Mark where platelets are.
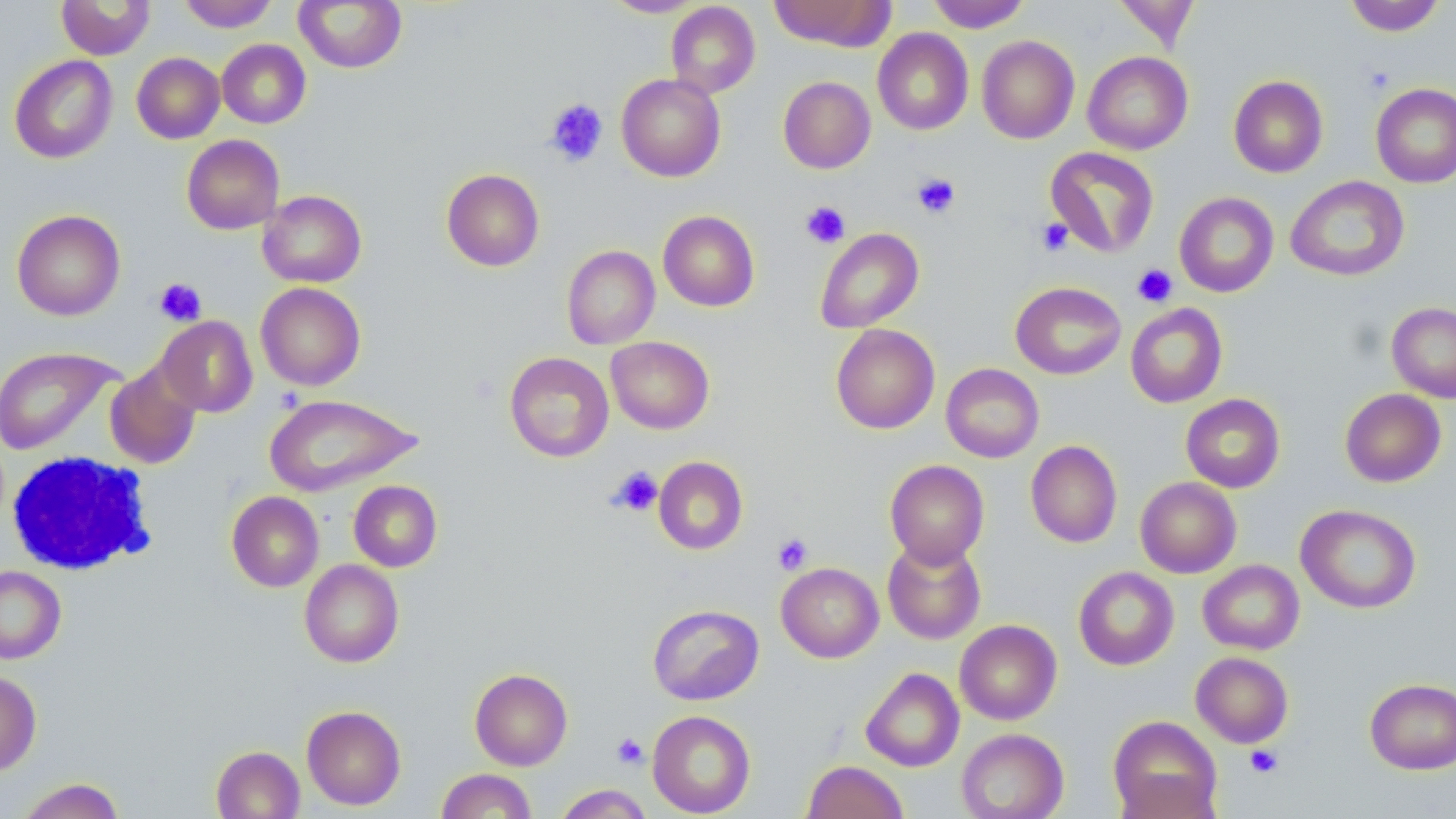
Approximate bounding boxes as named x1/y1/x2/y2 corners in pixels.
Platelets: (x1=544, y1=98, x2=609, y2=167), (x1=912, y1=173, x2=961, y2=219), (x1=800, y1=201, x2=850, y2=248), (x1=1036, y1=217, x2=1073, y2=256), (x1=1132, y1=264, x2=1177, y2=307), (x1=154, y1=277, x2=206, y2=326), (x1=609, y1=467, x2=663, y2=516), (x1=772, y1=533, x2=813, y2=575), (x1=612, y1=733, x2=648, y2=769), (x1=1245, y1=745, x2=1284, y2=778).

Summary:
  - White blood cell locations: (x1=5, y1=452, x2=156, y2=576)
  - Uninfected red blood cell locations: (x1=177, y1=0, x2=279, y2=31), (x1=295, y1=0, x2=406, y2=73), (x1=601, y1=0, x2=707, y2=17), (x1=769, y1=0, x2=894, y2=51), (x1=927, y1=0, x2=1031, y2=32), (x1=1112, y1=0, x2=1201, y2=51), (x1=1344, y1=0, x2=1446, y2=36), (x1=57, y1=1, x2=155, y2=60), (x1=666, y1=2, x2=760, y2=98), (x1=872, y1=28, x2=973, y2=135), (x1=977, y1=36, x2=1079, y2=144), (x1=217, y1=39, x2=311, y2=129), (x1=1082, y1=51, x2=1193, y2=154), (x1=131, y1=52, x2=225, y2=143), (x1=9, y1=55, x2=118, y2=163), (x1=616, y1=73, x2=726, y2=181), (x1=1228, y1=75, x2=1328, y2=178), (x1=778, y1=76, x2=876, y2=174), (x1=1371, y1=82, x2=1456, y2=188), (x1=181, y1=134, x2=284, y2=234), (x1=1045, y1=146, x2=1160, y2=257), (x1=442, y1=169, x2=544, y2=272), (x1=1286, y1=175, x2=1410, y2=282), (x1=258, y1=189, x2=367, y2=287), (x1=1174, y1=192, x2=1279, y2=298), (x1=11, y1=209, x2=125, y2=321), (x1=658, y1=210, x2=760, y2=311), (x1=814, y1=228, x2=924, y2=333), (x1=561, y1=245, x2=660, y2=349), (x1=1010, y1=281, x2=1126, y2=379), (x1=255, y1=282, x2=366, y2=390), (x1=1386, y1=301, x2=1456, y2=403), (x1=1125, y1=303, x2=1227, y2=408), (x1=156, y1=316, x2=258, y2=417), (x1=830, y1=324, x2=940, y2=434), (x1=606, y1=336, x2=715, y2=434), (x1=0, y1=346, x2=121, y2=455), (x1=504, y1=352, x2=614, y2=462), (x1=104, y1=362, x2=202, y2=470), (x1=941, y1=363, x2=1044, y2=463), (x1=1340, y1=388, x2=1447, y2=487), (x1=1180, y1=393, x2=1285, y2=493), (x1=264, y1=394, x2=422, y2=497), (x1=1025, y1=440, x2=1122, y2=547), (x1=654, y1=456, x2=748, y2=555), (x1=885, y1=459, x2=989, y2=567), (x1=1135, y1=476, x2=1241, y2=578), (x1=348, y1=480, x2=442, y2=571), (x1=226, y1=491, x2=324, y2=592), (x1=1295, y1=504, x2=1422, y2=614), (x1=882, y1=538, x2=986, y2=645), (x1=299, y1=559, x2=404, y2=667), (x1=1198, y1=560, x2=1304, y2=654), (x1=776, y1=562, x2=884, y2=663), (x1=0, y1=565, x2=66, y2=664), (x1=1073, y1=566, x2=1179, y2=670), (x1=647, y1=604, x2=764, y2=705), (x1=955, y1=620, x2=1062, y2=724), (x1=1191, y1=652, x2=1294, y2=748), (x1=861, y1=667, x2=964, y2=772), (x1=469, y1=668, x2=573, y2=770), (x1=0, y1=670, x2=41, y2=775), (x1=1364, y1=678, x2=1456, y2=774), (x1=301, y1=705, x2=406, y2=810), (x1=647, y1=710, x2=756, y2=817), (x1=1108, y1=716, x2=1222, y2=818), (x1=956, y1=728, x2=1069, y2=819), (x1=211, y1=745, x2=305, y2=819), (x1=802, y1=761, x2=908, y2=819), (x1=436, y1=768, x2=537, y2=818), (x1=1114, y1=771, x2=1221, y2=819), (x1=17, y1=778, x2=124, y2=819), (x1=553, y1=784, x2=653, y2=818)
  - Slide-level diagnosis: negative for blood parasites
  - Stain: May-Grünwald-Giemsa
  - Image size: 1456×819 pixels
  - Magnification: 1000x
  - Preparation: thin blood film
  - Field of view: one of a larger specimen
  - Modality: optical microscopy